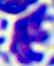
modality = micrograph
identification = white blood cell
magnification = 400x